Classify this cell by malaria status.
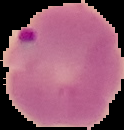
Parasitized.

From a thin blood smear. Segmented cell region on a black background. Image is 124×130 pixels.